Outline each blood parasite and name the species.
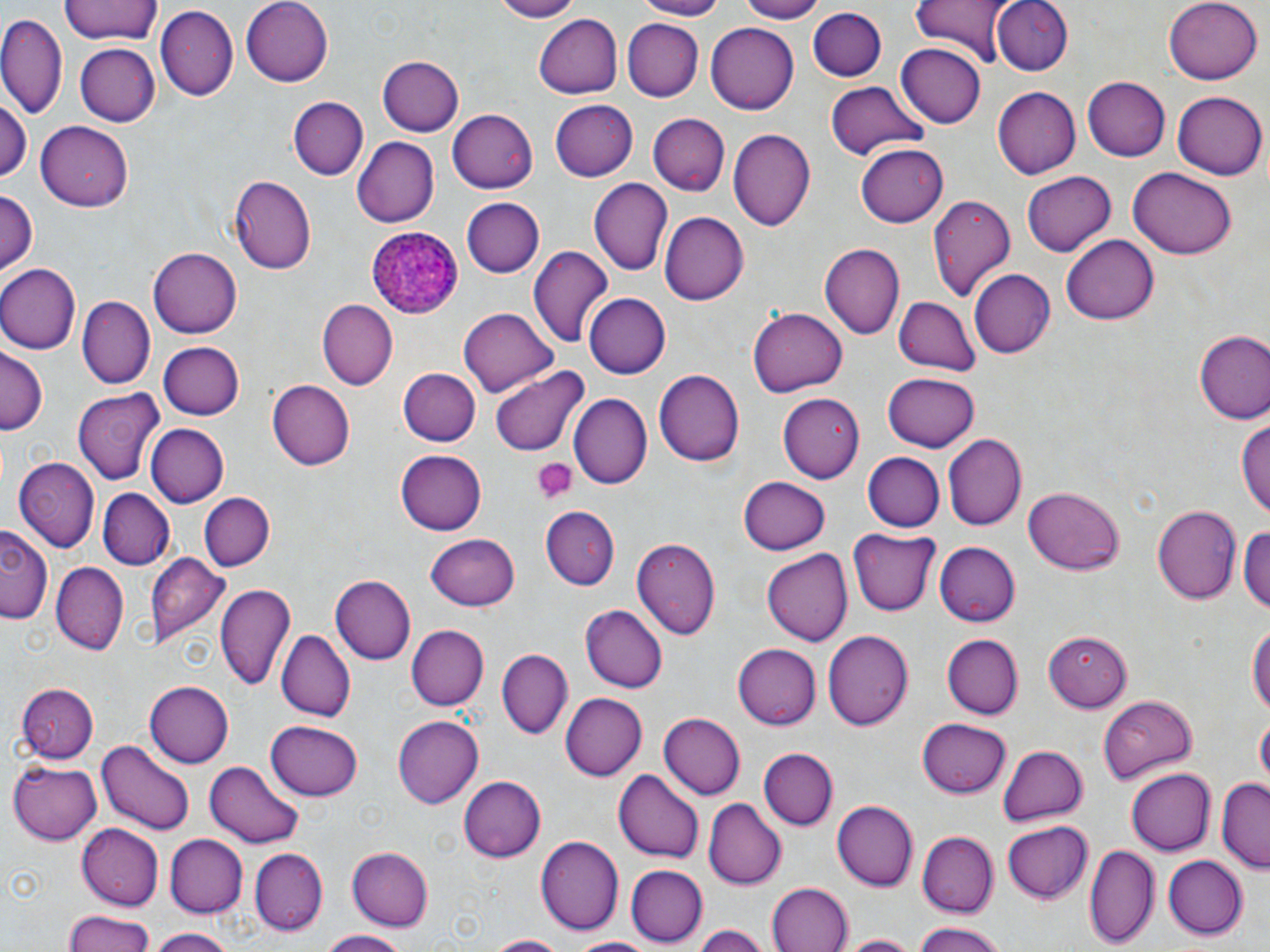

Approximate bounding boxes as [x1, y1, x2, y2] in pixels.
Plasmodium ovale-infected red blood cells: [364, 222, 462, 319].
No Plasmodium falciparum, Plasmodium malariae, Plasmodium vivax, Babesia divergens, or Trypanosoma brucei observed.

slide_level_diagnosis: Plasmodium ovale
magnification: 1000x
preparation: thin blood film
uninfected_red_blood_cell_locations: 'approximate bounding boxes as [x1, y1, x2, y2] in pixels: [60, 0, 163, 45], [243, 0, 336, 84], [482, 0, 585, 22], [631, 0, 728, 20], [737, 0, 822, 22], [990, 0, 1073, 73], [1163, 0, 1262, 84], [909, 1, 1014, 64], [806, 6, 886, 81], [156, 7, 237, 102], [532, 12, 622, 99], [0, 15, 68, 120], [621, 18, 702, 100], [706, 24, 799, 113], [75, 43, 160, 126], [896, 43, 986, 129], [377, 56, 462, 137], [1084, 76, 1170, 162], [826, 80, 928, 161], [993, 87, 1080, 179], [1172, 90, 1266, 179], [0, 95, 31, 183], [288, 96, 367, 180], [549, 97, 638, 180], [449, 108, 538, 194], [647, 112, 730, 196], [35, 121, 135, 211], [728, 129, 814, 233], [352, 136, 438, 228], [856, 142, 948, 228], [1128, 167, 1237, 260], [1022, 170, 1116, 258], [229, 177, 316, 273], [589, 177, 672, 275], [0, 189, 37, 279], [927, 192, 1017, 300], [459, 196, 543, 276], [660, 212, 749, 304], [1061, 233, 1161, 324], [821, 244, 903, 339], [527, 245, 614, 350], [148, 248, 243, 338], [0, 264, 79, 354], [968, 270, 1054, 359], [582, 292, 670, 379], [77, 295, 155, 389], [893, 298, 982, 375], [317, 299, 397, 390], [460, 307, 558, 396], [748, 308, 848, 397], [1194, 332, 1270, 425], [156, 341, 243, 420], [0, 349, 44, 435], [398, 366, 479, 446], [488, 366, 590, 457], [656, 368, 747, 466], [883, 371, 979, 452], [266, 379, 355, 470], [72, 387, 165, 485], [777, 392, 863, 484], [568, 394, 652, 490], [1239, 413, 1270, 523], [144, 423, 227, 509], [944, 433, 1027, 532], [394, 449, 487, 535], [862, 452, 944, 531], [13, 457, 100, 550], [739, 476, 831, 554], [1023, 487, 1124, 576], [98, 489, 173, 570], [198, 493, 272, 573], [1152, 503, 1242, 605], [542, 504, 619, 589], [1242, 521, 1270, 616], [0, 526, 51, 624], [849, 529, 940, 616], [426, 534, 521, 611], [631, 536, 721, 640], [933, 541, 1020, 627], [764, 548, 853, 647], [146, 552, 229, 647], [51, 560, 129, 652], [330, 575, 415, 665], [215, 581, 294, 694], [581, 605, 668, 693], [1247, 619, 1270, 725], [407, 626, 488, 711], [275, 628, 352, 722], [822, 629, 912, 732], [1044, 631, 1131, 712], [941, 634, 1021, 720], [734, 642, 820, 730], [497, 647, 572, 738], [143, 680, 232, 769], [19, 684, 96, 763], [559, 692, 644, 781], [1098, 693, 1198, 782], [391, 713, 482, 806], [659, 713, 745, 801], [1256, 716, 1269, 788], [918, 717, 1010, 798], [265, 720, 362, 801], [214, 724, 354, 825], [96, 740, 195, 836], [996, 744, 1087, 827], [759, 748, 839, 830], [8, 761, 101, 845], [203, 761, 307, 847], [613, 768, 704, 864], [1126, 769, 1216, 855], [457, 775, 545, 864], [1216, 779, 1269, 870], [703, 800, 784, 889], [832, 800, 918, 890], [1002, 822, 1094, 904], [76, 824, 165, 908], [917, 831, 996, 916], [165, 835, 247, 917], [536, 835, 623, 936], [1088, 843, 1159, 951], [346, 845, 433, 931], [250, 849, 327, 935], [1161, 854, 1247, 939], [625, 866, 707, 946], [766, 883, 854, 952], [61, 909, 159, 952], [908, 922, 1012, 952], [689, 924, 771, 952], [146, 927, 241, 952], [317, 930, 410, 952], [836, 933, 925, 952], [484, 934, 567, 952], [563, 936, 664, 952]'
platelet_locations: 'approximate bounding boxes as [x1, y1, x2, y2] in pixels: [533, 459, 575, 504]'
image_size: 1270×952 pixels
field_of_view: one of a larger specimen
stain: May-Grünwald-Giemsa
modality: light microscopy